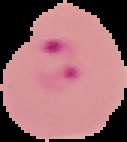
Malaria status: parasitized. Image is 127×142 pixels. Cell region segmented out of the field of view; the surrounding area is masked to black. From a thin blood smear.